Locate every Plasmodium parasite.
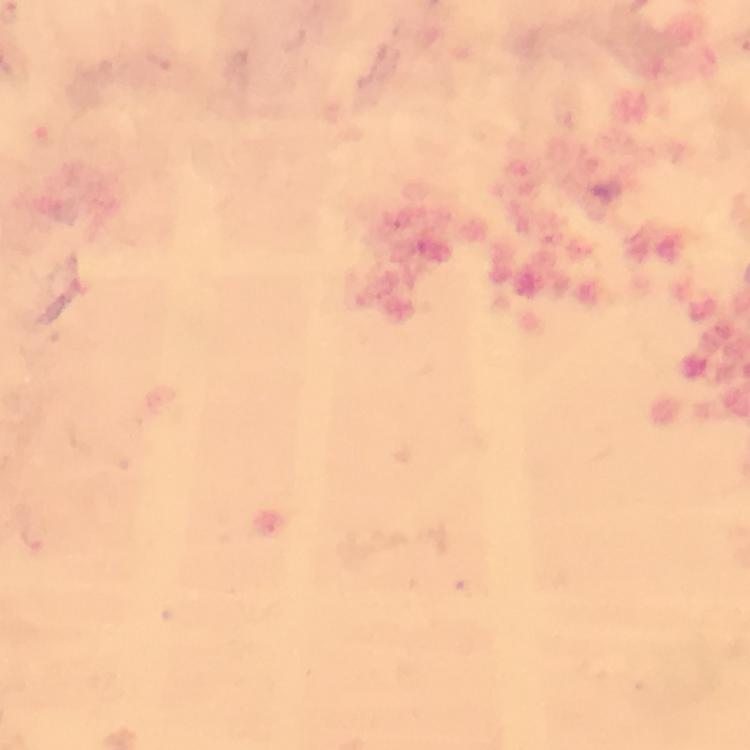
Approximate centers as {x, y} in pixels.
Plasmodium parasites: {47, 137}.

Summary:
  - Magnification: 100x
  - Stain: Giemsa
  - Cropped from: a single field of view
  - Preparation: thick blood film
  - Capture: smartphone camera through the microscope
  - Context: from a malaria diagnostic workup
  - Image size: 750×750 pixels
  - Immersion oil: used